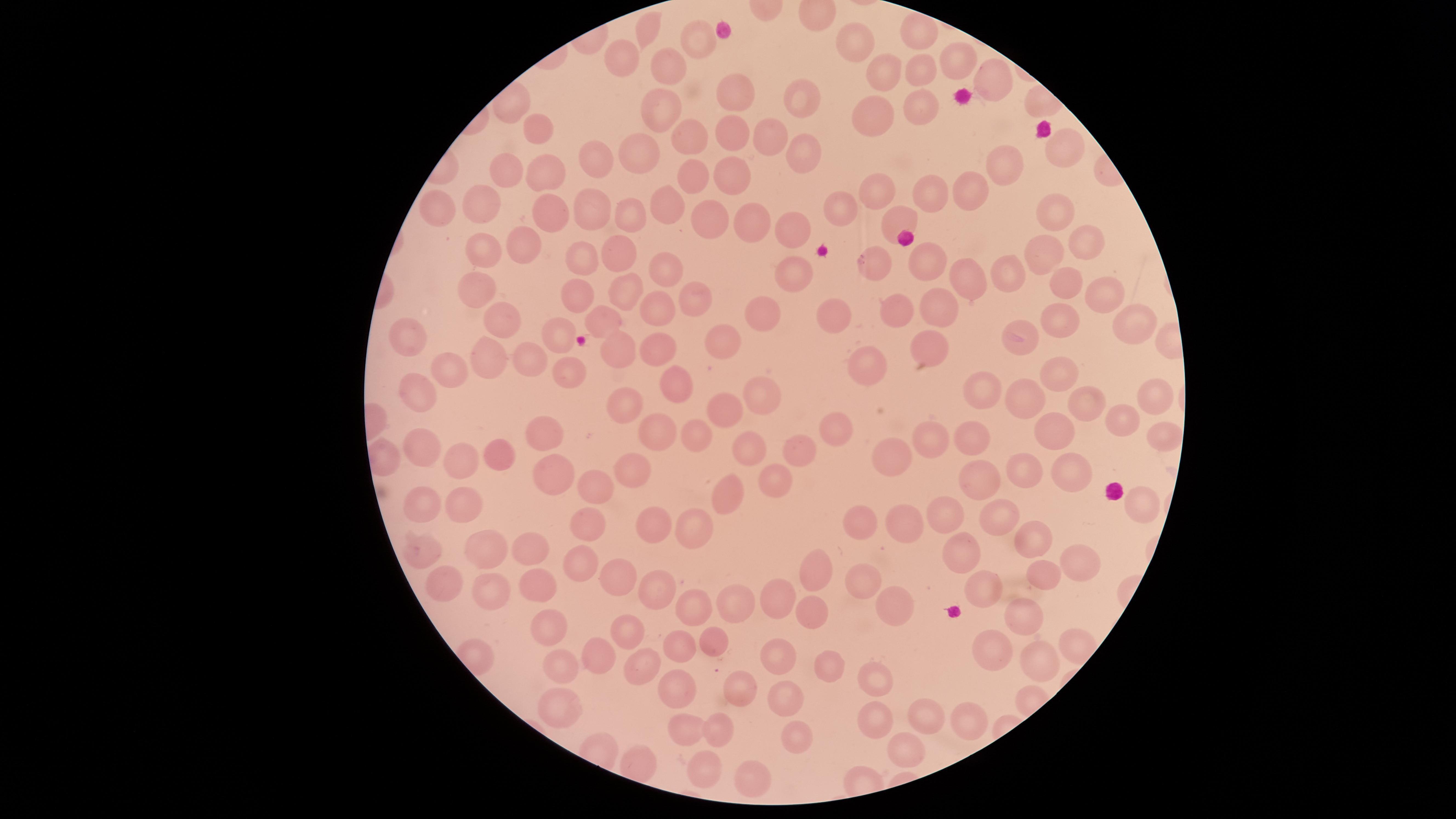
Approximate marker points as {x, y} in pixels.
Summary:
  - Uninfected red blood cells: {644, 28}, {916, 30}, {698, 37}, {857, 39}, {619, 51}, {955, 65}, {662, 70}, {923, 74}, {888, 77}, {995, 77}, {733, 93}, {804, 98}, {924, 99}, {660, 111}, {879, 117}, {729, 130}, {541, 135}, {768, 138}, {688, 140}, {1064, 144}, {639, 149}, {800, 153}, {592, 162}, {502, 170}, {732, 171}, {1004, 171}, {544, 174}, {692, 176}, {873, 188}, {978, 190}, {932, 194}, {672, 200}, {481, 201}, {442, 203}, {840, 205}, {592, 206}, {547, 212}, {1055, 212}, {633, 213}, {899, 215}, {708, 223}, {748, 224}, {791, 230}, {1080, 240}, {482, 244}, {526, 246}, {623, 250}, {1043, 258}, {586, 260}, {876, 260}, {926, 265}, {663, 267}, {1014, 275}, {792, 276}, {972, 278}, {478, 284}, {1063, 285}, {626, 290}, {577, 296}, {1105, 296}, {697, 298}, {660, 306}, {763, 308}, {947, 309}, {825, 310}, {889, 314}, {1054, 316}, {1133, 320}, {505, 321}, {605, 323}, {410, 327}, {559, 330}, {723, 338}, {1020, 338}, {655, 341}, {930, 344}, {490, 350}, {616, 353}, {535, 362}, {867, 362}, {458, 363}, {567, 368}, {675, 378}, {420, 379}, {1066, 380}, {988, 389}, {1028, 392}, {1152, 393}, {766, 396}, {633, 398}, {1092, 401}, {721, 405}, {1123, 417}, {1059, 424}, {840, 427}, {970, 430}, {540, 431}, {656, 432}, {696, 434}, {936, 434}, {1152, 435}, {425, 447}, {798, 450}, {747, 451}, {506, 456}, {892, 456}, {469, 464}, {556, 468}, {630, 472}, {1026, 474}, {1068, 474}, {777, 481}, {984, 481}, {592, 484}, {731, 497}, {421, 503}, {1135, 503}, {467, 506}, {949, 515}, {1001, 519}, {859, 522}, {905, 522}, {650, 525}, {587, 527}, {697, 527}, {1027, 539}, {419, 548}, {533, 548}, {966, 548}, {485, 554}, {1068, 556}, {581, 559}, {814, 572}, {621, 577}, {1045, 577}, {862, 580}, {439, 585}, {533, 585}, {655, 589}, {985, 590}, {782, 592}, {489, 597}, {890, 600}, {744, 602}, {696, 606}, {1022, 612}, {814, 615}, {550, 620}, {628, 634}, {719, 642}, {678, 644}, {997, 647}, {598, 655}, {777, 656}, {1039, 660}, {642, 661}, {822, 665}, {561, 668}, {873, 676}, {685, 686}, {736, 691}, {784, 701}, {562, 705}, {922, 714}, {969, 718}, {875, 719}, {725, 726}, {686, 733}, {789, 735}, {906, 743}, {701, 769}, {757, 776}
  - Capture: smartphone photograph through the microscope eyepiece
  - Visible region: circular
  - Preparation: thin blood smear
  - Stain: Giemsa
  - Presence: no malaria parasites identified
  - Field of view: single
  - Image size: 1456×819 pixels